Point out each leukocyte.
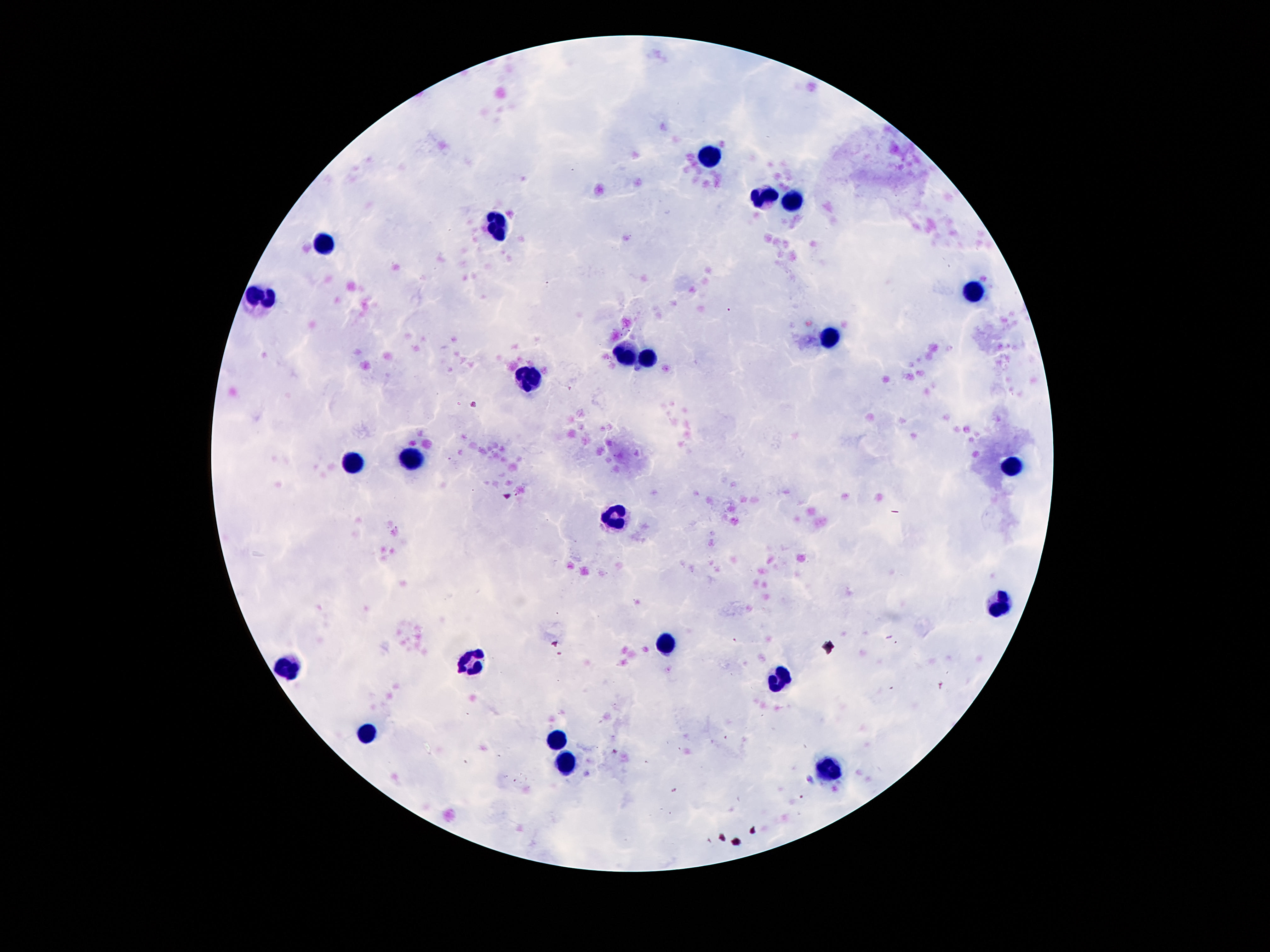

Approximate centers as [x, y] in pixels.
Leukocytes: [711, 157], [765, 196], [793, 199], [498, 226], [323, 245], [972, 290], [263, 299], [830, 338], [625, 352], [648, 358], [527, 379], [412, 459], [356, 460], [1012, 466], [618, 518], [996, 601], [669, 645], [470, 660], [288, 669], [781, 678], [366, 734], [555, 741], [569, 759], [825, 769].

Summary:
  - Field of view: one from this slide
  - Magnification: 100x
  - Preparation: thick blood film
  - Stain: Giemsa
  - Patient malaria status: uninfected
  - Image size: 1270×952 pixels
  - Capture: smartphone camera through the microscope eyepiece